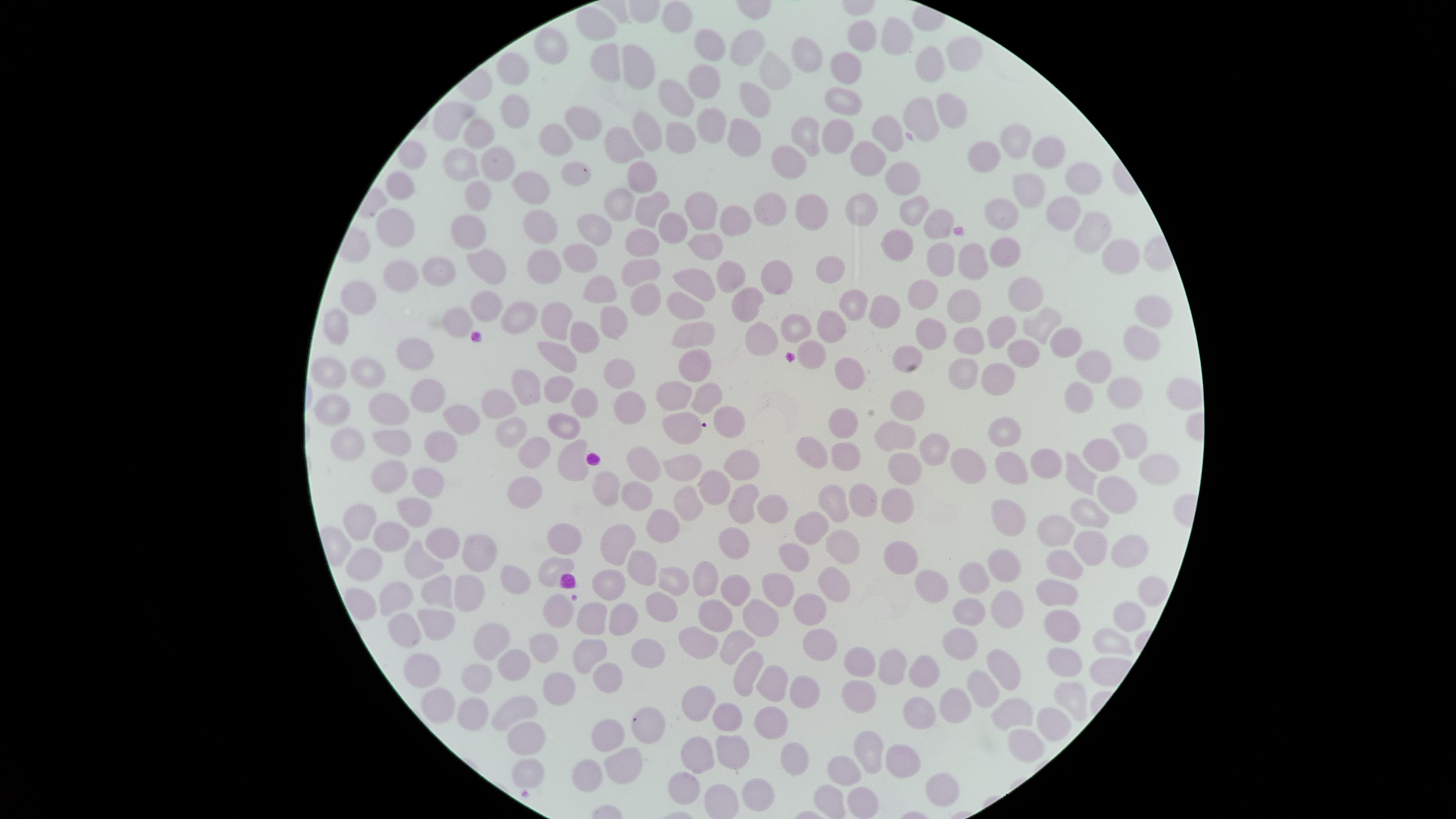 Approximate marker points as {x, y} in pixels. Uninfected RBCs: {676, 17}, {592, 25}, {889, 34}, {741, 41}, {855, 42}, {715, 45}, {552, 52}, {811, 53}, {958, 55}, {603, 60}, {638, 67}, {927, 67}, {775, 68}, {845, 68}, {518, 70}, {707, 79}, {748, 95}, {843, 99}, {675, 100}, {949, 109}, {518, 112}, {450, 118}, {576, 118}, {707, 121}, {919, 122}, {881, 127}, {643, 128}, {736, 131}, {810, 131}, {831, 132}, {477, 133}, {679, 134}, {560, 136}, {1012, 137}, {618, 139}, {412, 147}, {1045, 151}, {982, 155}, {496, 161}, {799, 161}, {459, 163}, {868, 163}, {582, 171}, {403, 176}, {907, 179}, {1080, 179}, {643, 180}, {535, 188}, {1026, 195}, {480, 197}, {615, 204}, {651, 204}, {698, 206}, {770, 208}, {914, 208}, {859, 209}, {816, 210}, {1001, 211}, {1060, 214}, {937, 221}, {729, 222}, {543, 223}, {674, 224}, {399, 231}, {1091, 233}, {470, 235}, {595, 235}, {643, 239}, {705, 245}, {898, 245}, {1005, 249}, {573, 251}, {1119, 257}, {486, 258}, {939, 258}, {979, 260}, {543, 264}, {832, 264}, {442, 267}, {636, 268}, {725, 269}, {777, 271}, {396, 276}, {698, 280}, {603, 290}, {1021, 291}, {356, 295}, {920, 296}, {644, 300}, {486, 303}, {744, 304}, {851, 304}, {965, 304}, {690, 309}, {887, 309}, {1156, 313}, {553, 319}, {1038, 320}, {612, 322}, {794, 322}, {331, 323}, {450, 326}, {1003, 329}, {828, 333}, {933, 333}, {582, 336}, {699, 336}, {762, 338}, {1065, 340}, {1139, 343}, {970, 345}, {555, 347}, {810, 351}, {908, 352}, {421, 355}, {1022, 356}, {695, 364}, {1094, 364}, {614, 368}, {377, 369}, {342, 371}, {963, 373}, {851, 374}, {994, 375}, {529, 385}, {558, 391}, {1079, 392}, {667, 393}, {1177, 393}, {1129, 394}, {425, 396}, {709, 396}, {495, 398}, {585, 399}, {620, 401}, {908, 403}, {336, 405}, {379, 407}, {462, 414}, {726, 419}, {845, 419}, {568, 424}, {681, 424}, {1002, 429}, {893, 433}, {506, 435}, {926, 440}, {1133, 440}, {399, 441}, {352, 442}, {445, 442}, {812, 443}, {844, 452}, {530, 455}, {573, 455}, {1102, 456}, {643, 458}, {745, 462}, {899, 462}, {1043, 462}, {975, 466}, {393, 467}, {1016, 470}, {1152, 470}, {686, 471}, {423, 477}, {1081, 477}, {717, 484}, {605, 489}, {1113, 491}, {530, 494}, {638, 496}, {861, 498}, {832, 500}, {893, 501}, {689, 503}, {741, 503}, {407, 504}, {771, 510}, {1003, 510}, {1085, 510}, {365, 518}, {809, 522}, {665, 524}, {1055, 528}, {565, 531}, {388, 536}, {442, 540}, {1091, 543}, {731, 545}, {843, 545}, {616, 546}, {1125, 548}, {471, 552}, {791, 556}, {900, 560}, {1070, 562}, {423, 563}, {1002, 563}, {369, 564}, {553, 564}, {643, 568}, {708, 574}, {973, 576}, {674, 577}, {828, 579}, {522, 582}, {604, 582}, {937, 582}, {776, 583}, {435, 588}, {463, 588}, {1065, 589}, {735, 591}, {397, 595}, {660, 602}, {1004, 606}, {812, 610}, {556, 612}, {626, 613}, {716, 613}, {591, 615}, {968, 616}, {761, 619}, {1127, 621}, {1055, 622}, {435, 624}, {400, 629}, {697, 633}, {492, 636}, {740, 639}, {959, 639}, {1110, 640}, {813, 643}, {542, 646}, {587, 648}, {642, 652}, {858, 661}, {1068, 666}, {893, 667}, {743, 668}, {998, 670}, {514, 672}, {421, 673}, {476, 674}, {926, 675}, {604, 679}, {769, 682}, {979, 686}, {557, 688}, {801, 688}, {864, 693}, {1073, 693}, {954, 701}, {699, 703}, {520, 710}, {435, 711}, {474, 711}, {1015, 711}, {919, 714}, {728, 715}, {773, 716}, {1051, 719}, {649, 722}, {606, 730}, {1026, 738}, {522, 740}, {866, 748}, {729, 752}, {699, 755}, {781, 758}, {903, 761}, {624, 765}, {839, 767}, {524, 771}, {586, 771}, {685, 775}, {758, 791}, {829, 791}, {934, 791}, {861, 800}. Smartphone photograph through the microscope eyepiece. Presence: no malaria parasites detected. Image is 1456×819 pixels. Single field of view. Thin blood film. Giemsa stain. The visible region is circular.